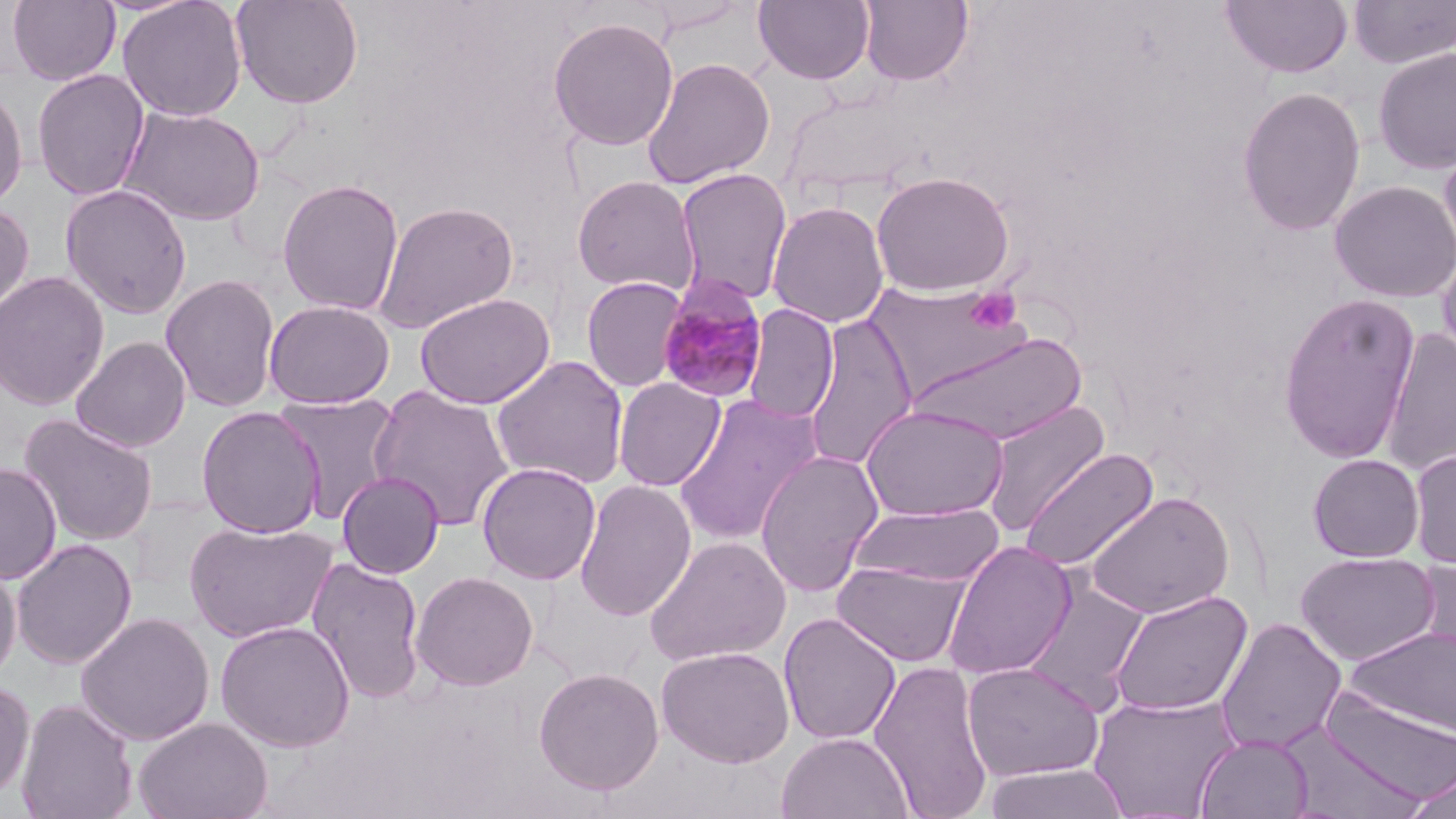 Approximate bounding boxes as [x1, y1, x2, y2] in pixels. Uninfected red blood cell locations: [7, 0, 121, 86], [117, 0, 248, 122], [230, 0, 364, 110], [753, 0, 876, 85], [1219, 0, 1354, 79], [857, 1, 973, 87], [1347, 1, 1456, 69], [547, 16, 679, 151], [1372, 45, 1456, 175], [641, 56, 776, 189], [31, 68, 150, 201], [0, 84, 28, 209], [1236, 86, 1366, 237], [119, 105, 266, 227], [1438, 136, 1456, 271], [675, 167, 792, 306], [871, 170, 1014, 296], [571, 175, 701, 297], [277, 179, 404, 316], [1329, 180, 1456, 303], [60, 183, 193, 319], [373, 200, 519, 334], [767, 200, 889, 328], [0, 204, 35, 316], [1436, 245, 1456, 372], [0, 270, 110, 410], [160, 274, 281, 412], [581, 276, 688, 392], [864, 282, 1028, 399], [414, 292, 556, 409], [1277, 292, 1421, 464], [263, 299, 396, 409], [742, 304, 840, 424], [803, 313, 919, 472], [1380, 327, 1456, 477], [908, 329, 1088, 446], [71, 336, 192, 452], [490, 355, 629, 490], [612, 376, 727, 491], [367, 385, 516, 531], [273, 392, 404, 524], [672, 395, 822, 547], [979, 399, 1111, 537], [861, 404, 1009, 522], [196, 406, 325, 539], [20, 413, 159, 547], [1409, 447, 1456, 569], [1018, 448, 1159, 572], [754, 450, 884, 598], [1308, 453, 1424, 562], [477, 461, 601, 585], [0, 463, 61, 584], [337, 470, 445, 579], [574, 480, 697, 621], [1085, 491, 1235, 620], [848, 502, 1007, 588], [183, 520, 339, 643], [644, 535, 792, 667], [11, 538, 137, 670], [942, 540, 1078, 680], [1295, 551, 1439, 667], [1413, 556, 1456, 671], [0, 558, 21, 684], [309, 558, 426, 703], [832, 560, 972, 668], [410, 571, 539, 691], [1019, 579, 1150, 713], [1107, 590, 1252, 716], [75, 611, 215, 746], [778, 613, 902, 745], [1215, 617, 1347, 754], [215, 620, 355, 752], [1347, 625, 1456, 739], [656, 646, 795, 767], [869, 658, 994, 819], [962, 661, 1104, 782], [532, 666, 665, 796], [0, 678, 35, 804], [1319, 686, 1456, 804], [1088, 692, 1242, 817], [16, 698, 138, 819], [133, 716, 273, 819], [1276, 726, 1431, 818], [776, 731, 914, 819], [1195, 733, 1315, 818], [982, 764, 1131, 819], [1398, 772, 1456, 819]. Platelet locations: [964, 287, 1022, 334]. Plasmodium malariae-infected red blood cell locations: [656, 276, 769, 404]. Slide-level diagnosis: Plasmodium malariae. Captured at 1000x magnification. May-Grünwald-Giemsa stain. Image is 1456×819 pixels. Single field of view. Light microscopy. Thin blood smear.